Classify this cell by malaria status.
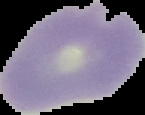
It is uninfected.

{
  "image_size": "145×115 pixels",
  "preparation": "thin blood film",
  "image_type": "segmented cell region with the area outside set to black"
}